Locate every blood parasite and identify its species.
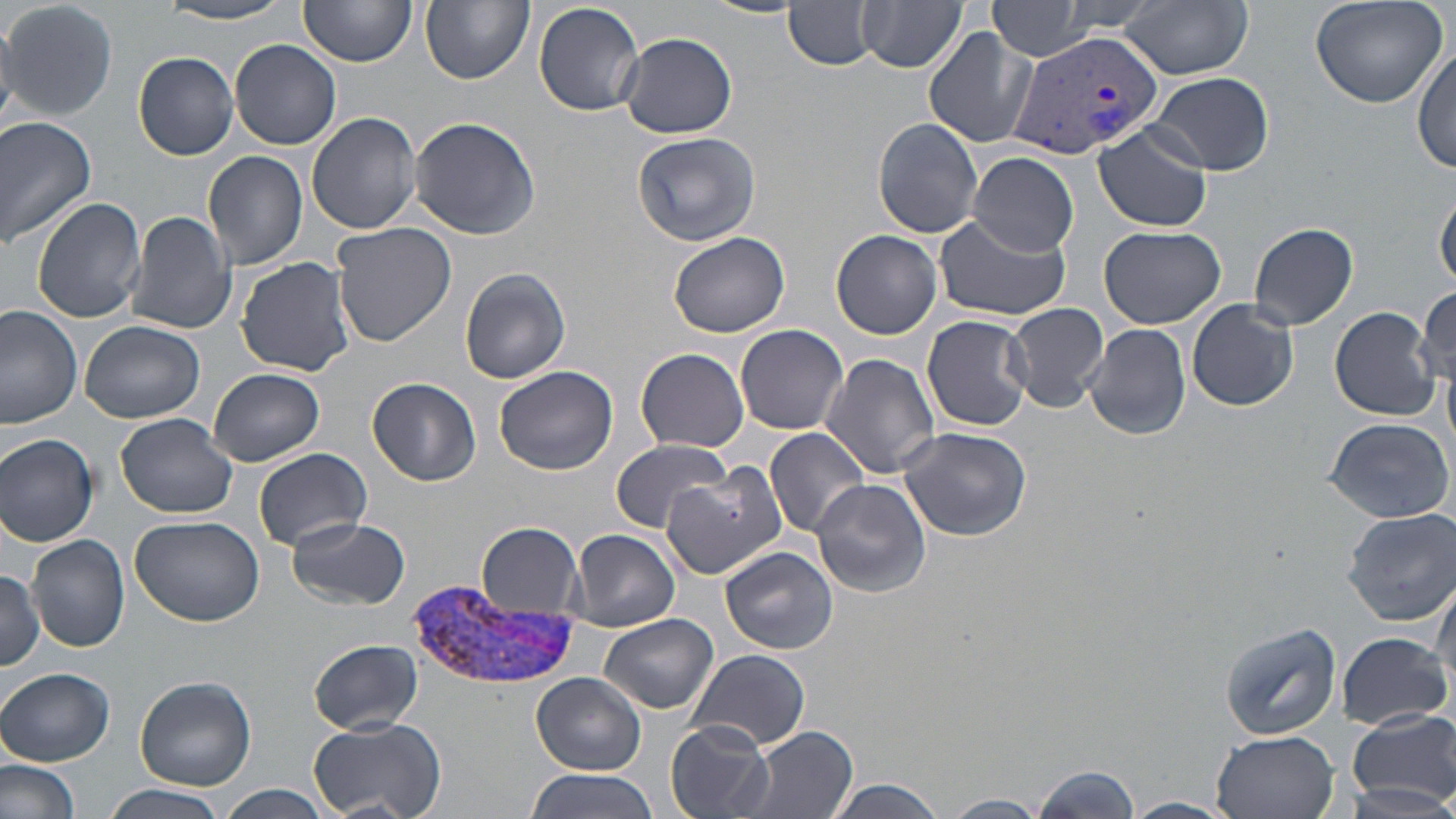

Approximate bounding boxes as (x1,y1)-(x2,y2) corner pairs in pixels.
Plasmodium vivax-infected red blood cells: (1010,27)-(1163,161), (409,579)-(576,691).
No Plasmodium falciparum, Plasmodium ovale, Plasmodium malariae, Babesia divergens, or Trypanosoma brucei observed.

slide-level diagnosis = Plasmodium vivax
modality = optical microscopy
stain = May-Grünwald-Giemsa
preparation = thin blood smear
field of view = single
uninfected red blood cell locations = approximate bounding boxes as (x1,y1)-(x2,y2) corner pairs in pixels: (2,0)-(117,122), (299,0)-(416,70), (421,0)-(533,85), (985,0)-(1098,59), (1309,0)-(1449,109), (532,1)-(647,117), (699,1)-(806,19), (859,1)-(968,74), (1053,1)-(1168,34), (1119,1)-(1254,80), (154,3)-(300,25), (784,3)-(880,69), (923,28)-(1036,148), (617,31)-(737,138), (230,38)-(342,149), (1413,44)-(1456,175), (133,52)-(240,160), (1147,71)-(1275,176), (307,111)-(425,235), (0,114)-(99,249), (409,116)-(541,241), (873,117)-(984,238), (1094,121)-(1213,231), (632,130)-(762,246), (203,149)-(310,273), (970,152)-(1079,257), (1435,186)-(1456,290), (31,197)-(146,323), (126,210)-(238,335), (935,214)-(1069,321), (1249,221)-(1359,330), (329,222)-(457,351), (1098,225)-(1225,329), (832,230)-(943,339), (668,231)-(789,338), (235,256)-(357,378), (459,267)-(571,384), (1414,286)-(1454,392), (1188,299)-(1301,413), (1006,302)-(1109,412), (0,304)-(83,428), (1329,306)-(1442,420), (921,315)-(1032,432), (80,319)-(206,423), (735,323)-(850,435), (1083,324)-(1190,441), (636,347)-(749,453), (822,354)-(940,478), (494,365)-(618,475), (207,368)-(325,466), (368,378)-(480,486), (116,413)-(238,520), (1322,416)-(1453,523), (897,426)-(1032,540), (765,428)-(873,538), (1,433)-(100,546), (610,441)-(734,532), (254,447)-(371,552), (660,462)-(788,581), (810,477)-(932,598), (1344,508)-(1456,625), (129,514)-(264,627), (286,517)-(410,611), (477,522)-(584,616), (568,528)-(680,632), (26,534)-(131,655), (719,545)-(838,655), (0,568)-(46,669), (1431,570)-(1456,695), (599,614)-(719,714), (1218,620)-(1342,741), (1335,631)-(1452,729), (309,639)-(421,735), (687,649)-(811,751), (1,668)-(114,765), (532,672)-(647,777), (132,676)-(257,790), (1347,708)-(1455,807), (303,714)-(447,819), (667,721)-(775,818), (733,728)-(860,818), (1211,731)-(1337,818), (0,756)-(80,819), (1028,764)-(1142,818), (525,769)-(660,819), (823,778)-(948,818), (104,783)-(228,819), (214,783)-(333,819), (940,794)-(1052,818), (1120,799)-(1236,819)
magnification = 1000x
image size = 1456×819 pixels